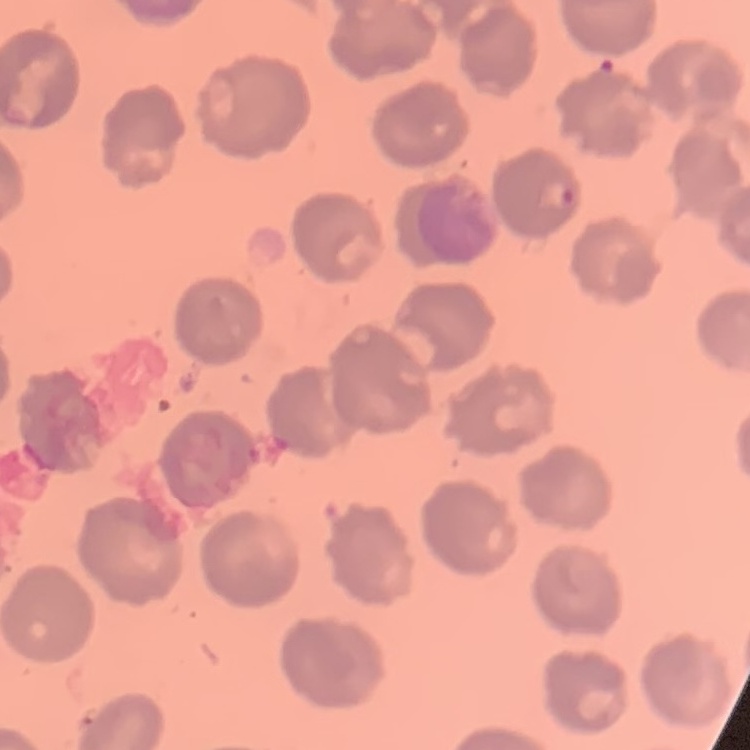 The erythrocytes exhibit no rouleaux formation. Field's or Giemsa stain. Square crop of a larger photomicrograph. Thin blood film.